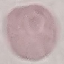
Summary:
  - Result: no malaria parasites detected
  - Image type: cell patch, automatically extracted from a larger field of view and resized to 64 × 64 pixels
  - Preparation: thin blood smear
  - Stain: Giemsa
  - Capture: smartphone through the microscope eyepiece